Report the malaria status of this cell.
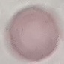

Uninfected.

Summary:
  - Capture: smartphone camera at the microscope eyepiece
  - Preparation: thin blood film
  - Stain: Giemsa
  - Image type: cell patch, automatically extracted from a larger field of view and resized to 64 × 64 pixels